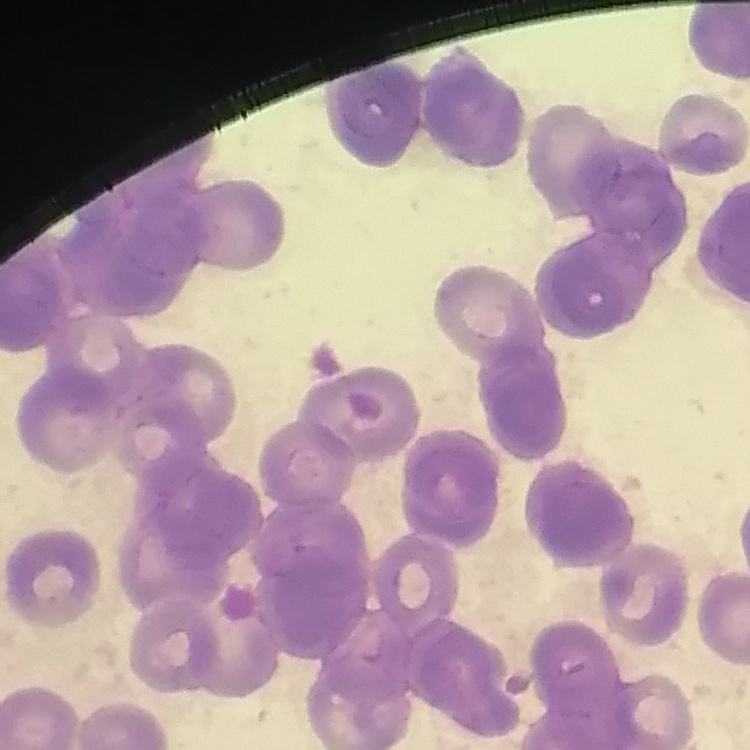

red_blood_cell_morphology: rouleaux formation
image_type: one tile cut from a larger photomicrograph
preparation: thin peripheral smear
stain: Field's or Giemsa